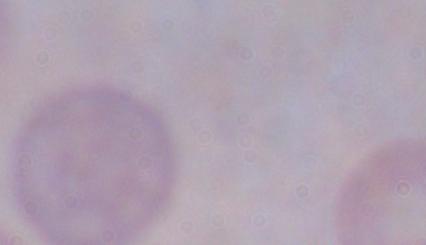

Summary:
  - Identification: trypanosome
  - Magnification: 1000x
  - Modality: photomicrograph